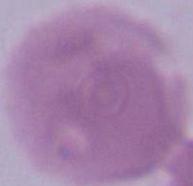

A red blood cell is seen. Photomicrograph. Captured at 1000x magnification.